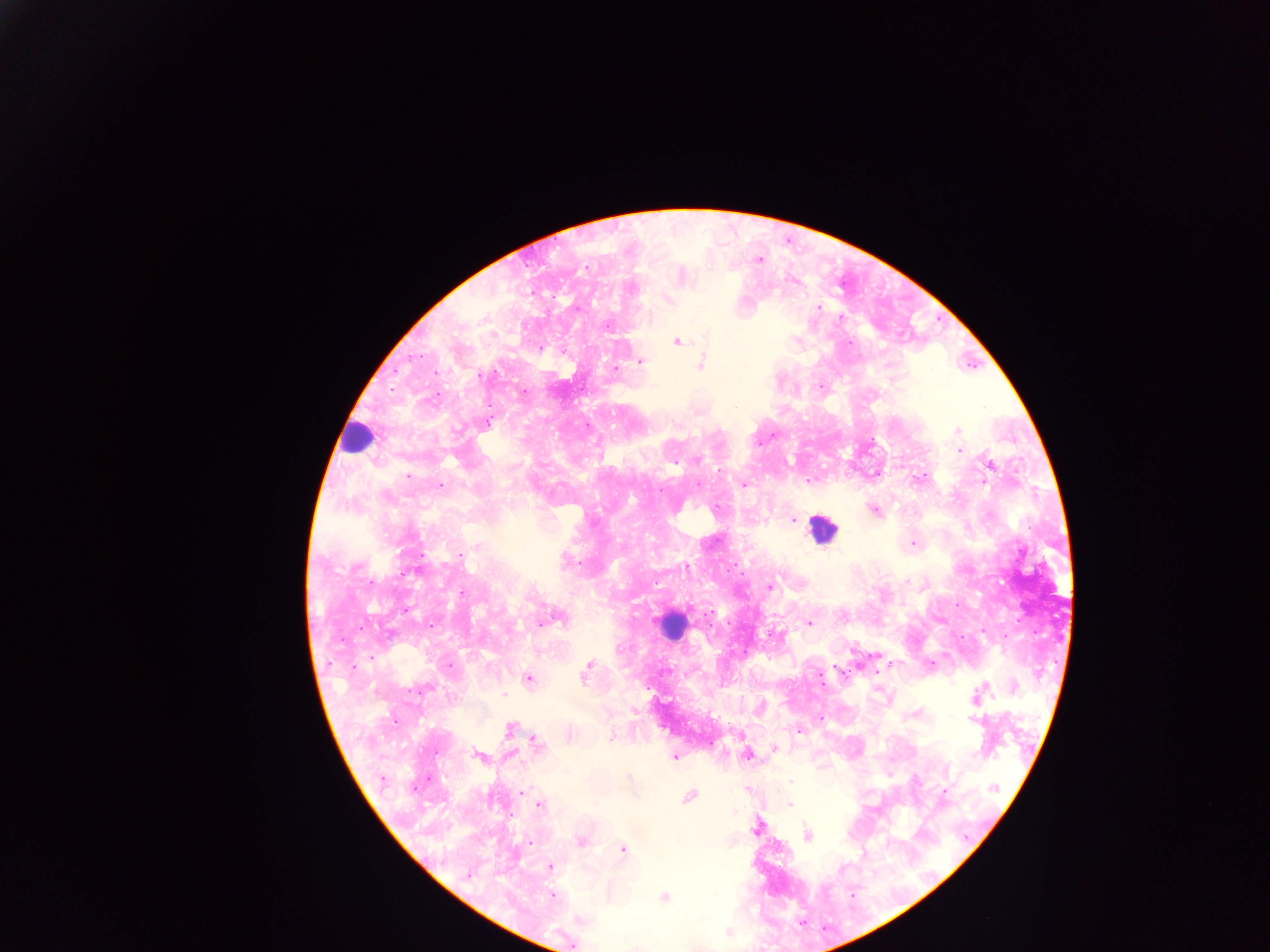
Approximate centers as (x, y) in pixels.
Summary:
  - Leukocyte locations: (358, 438), (823, 529), (670, 624)
  - Malaria parasite locations: (759, 259), (586, 266), (681, 275), (668, 298), (818, 307), (676, 341), (540, 348), (639, 360), (701, 364), (616, 370), (523, 392), (957, 431), (959, 450), (697, 459), (988, 464), (876, 473), (919, 478), (743, 485), (875, 511), (792, 519), (913, 543), (769, 586), (550, 618), (809, 623), (879, 655), (891, 664), (836, 666), (585, 672), (528, 678), (1012, 687), (976, 697), (760, 708), (819, 718), (975, 719), (509, 728), (798, 731), (568, 734), (535, 743), (774, 749), (747, 754), (479, 756), (673, 756), (747, 789), (943, 791), (521, 792), (689, 796), (539, 804), (788, 805), (756, 826), (807, 835), (580, 841), (622, 849), (549, 867), (469, 875), (552, 894), (663, 898), (726, 931), (571, 944)
  - Country: Ghana
  - Capture: mobile-phone photograph through a microscope
  - Field of view: single
  - Image size: 1270×952 pixels
  - Preparation: thick blood film